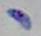
Summary:
  - Modality: photomicrograph
  - Identification: Toxoplasma gondii
  - Magnification: 1000x